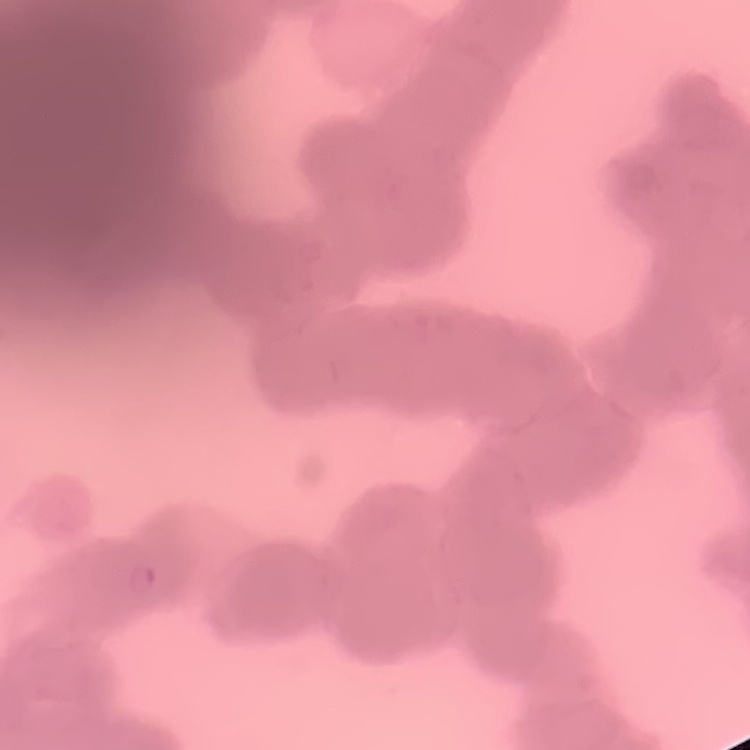

erythrocyte morphology = rouleaux formation
preparation = thin blood film
stain = Field's or Giemsa
image type = square crop of a larger photomicrograph